Assess the morphology of the red blood cells.
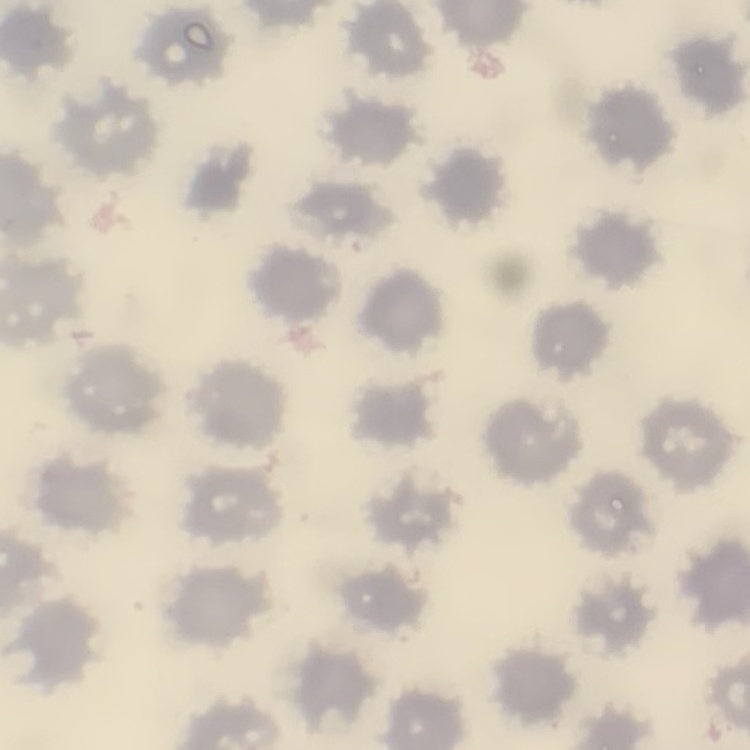
They show no rouleaux formation.

Summary:
  - Stain: Field's or Giemsa
  - Preparation: thin blood smear
  - Image type: one tile cut from a larger photomicrograph